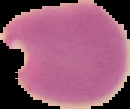

Summary:
  - Image type: segmented cell region with the area outside set to black
  - Malaria status: parasitized
  - Preparation: thin blood smear
  - Image size: 130×109 pixels